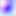

Summary:
  - Identification: Toxoplasma gondii
  - Magnification: 400x
  - Modality: micrograph